Find the red blood cells and label each as Plasmodium falciparum-infected, uninfected, or of indeterminate infection status.
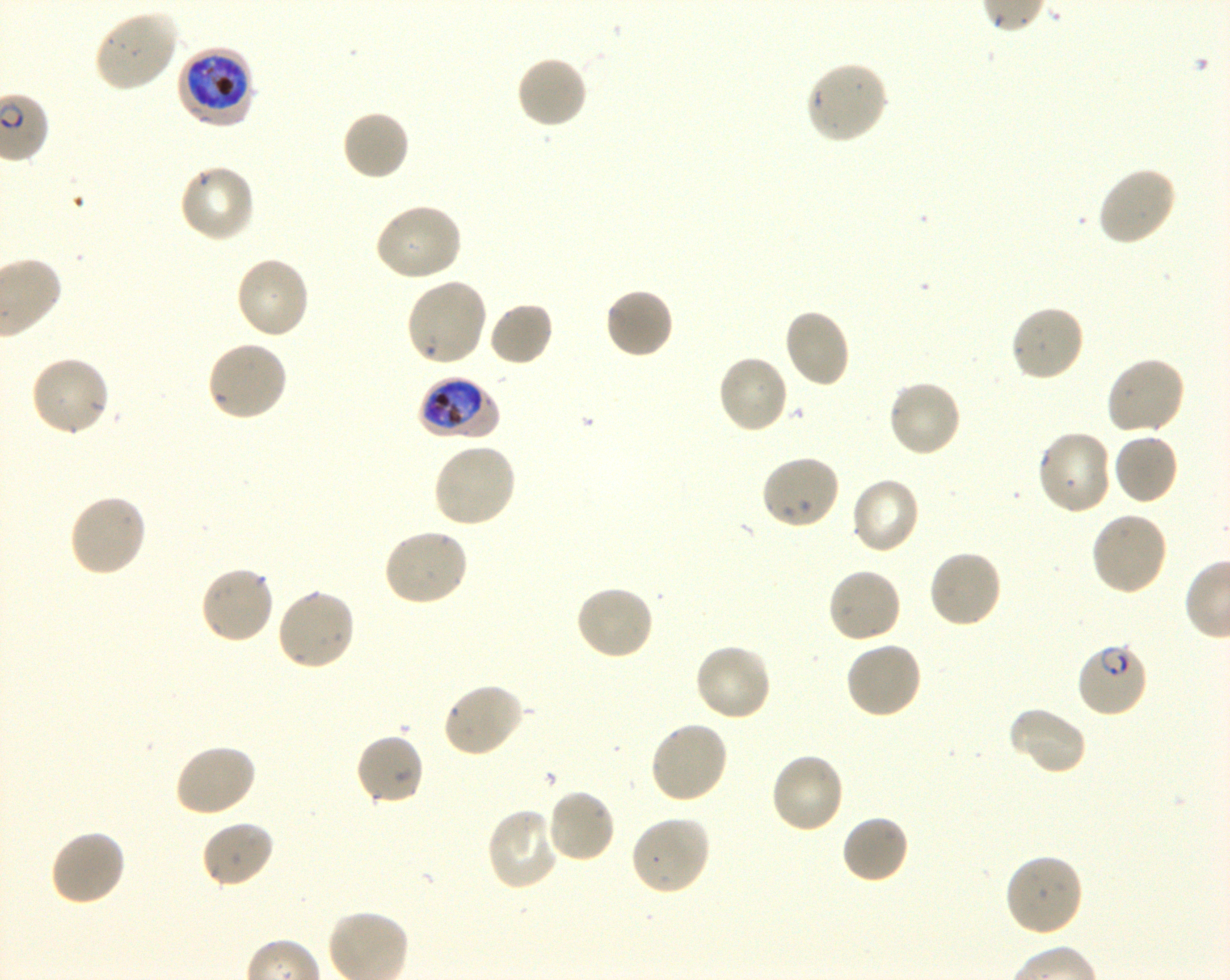
Approximate bounding rectangles given as corner coordinates in pixels from the top-left. Not every red blood cell is marked. A life-cycle stage — or a range of stages, where the recorded stages span more than one — follows each staged infected red blood cell.
Infected red blood cells: (x1=177, y1=45, x2=257, y2=128) early trophozoite to early schizont; (x1=418, y1=375, x2=498, y2=440) early trophozoite to early schizont; (x1=1074, y1=641, x2=1150, y2=719) ring.
Uninfected red blood cells: (x1=93, y1=9, x2=179, y2=93), (x1=515, y1=55, x2=589, y2=130), (x1=804, y1=59, x2=889, y2=145), (x1=341, y1=109, x2=412, y2=181), (x1=177, y1=163, x2=257, y2=243), (x1=1095, y1=165, x2=1178, y2=247), (x1=373, y1=202, x2=463, y2=282), (x1=234, y1=255, x2=310, y2=341), (x1=404, y1=277, x2=488, y2=368), (x1=604, y1=287, x2=675, y2=359), (x1=488, y1=301, x2=554, y2=368), (x1=1010, y1=303, x2=1086, y2=383), (x1=783, y1=307, x2=852, y2=390), (x1=206, y1=339, x2=289, y2=423), (x1=29, y1=354, x2=111, y2=437), (x1=716, y1=354, x2=789, y2=435), (x1=1104, y1=356, x2=1186, y2=437), (x1=886, y1=378, x2=964, y2=458), (x1=1035, y1=429, x2=1112, y2=516), (x1=1112, y1=431, x2=1179, y2=506), (x1=431, y1=441, x2=518, y2=529), (x1=758, y1=454, x2=840, y2=531), (x1=850, y1=476, x2=922, y2=555), (x1=67, y1=492, x2=147, y2=578), (x1=1090, y1=511, x2=1169, y2=596), (x1=381, y1=527, x2=469, y2=608), (x1=927, y1=549, x2=1004, y2=630), (x1=198, y1=564, x2=276, y2=645), (x1=826, y1=566, x2=903, y2=644), (x1=574, y1=583, x2=655, y2=661), (x1=275, y1=587, x2=357, y2=672), (x1=693, y1=641, x2=773, y2=722), (x1=844, y1=641, x2=923, y2=720), (x1=441, y1=681, x2=527, y2=759), (x1=1009, y1=705, x2=1087, y2=776), (x1=648, y1=719, x2=730, y2=805), (x1=354, y1=732, x2=425, y2=807), (x1=172, y1=742, x2=257, y2=818), (x1=769, y1=751, x2=846, y2=834), (x1=545, y1=789, x2=617, y2=865), (x1=485, y1=807, x2=562, y2=892), (x1=842, y1=813, x2=909, y2=885), (x1=629, y1=815, x2=712, y2=896), (x1=200, y1=820, x2=275, y2=889), (x1=48, y1=828, x2=127, y2=907), (x1=1003, y1=852, x2=1084, y2=938).
No red blood cells of indeterminate infection status observed.

culture = Plasmodium falciparum strain 3D7, shaking, in vitro
objective = 100x, oil immersion, numerical aperture 1.30
image size = 1230×980 pixels
donor blood group = O+
stain = Giemsa
preparation = thin blood film
field of view = single